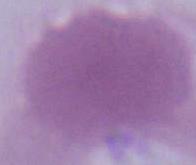

Captured at 1000x magnification. Photomicrograph. A red blood cell is seen.